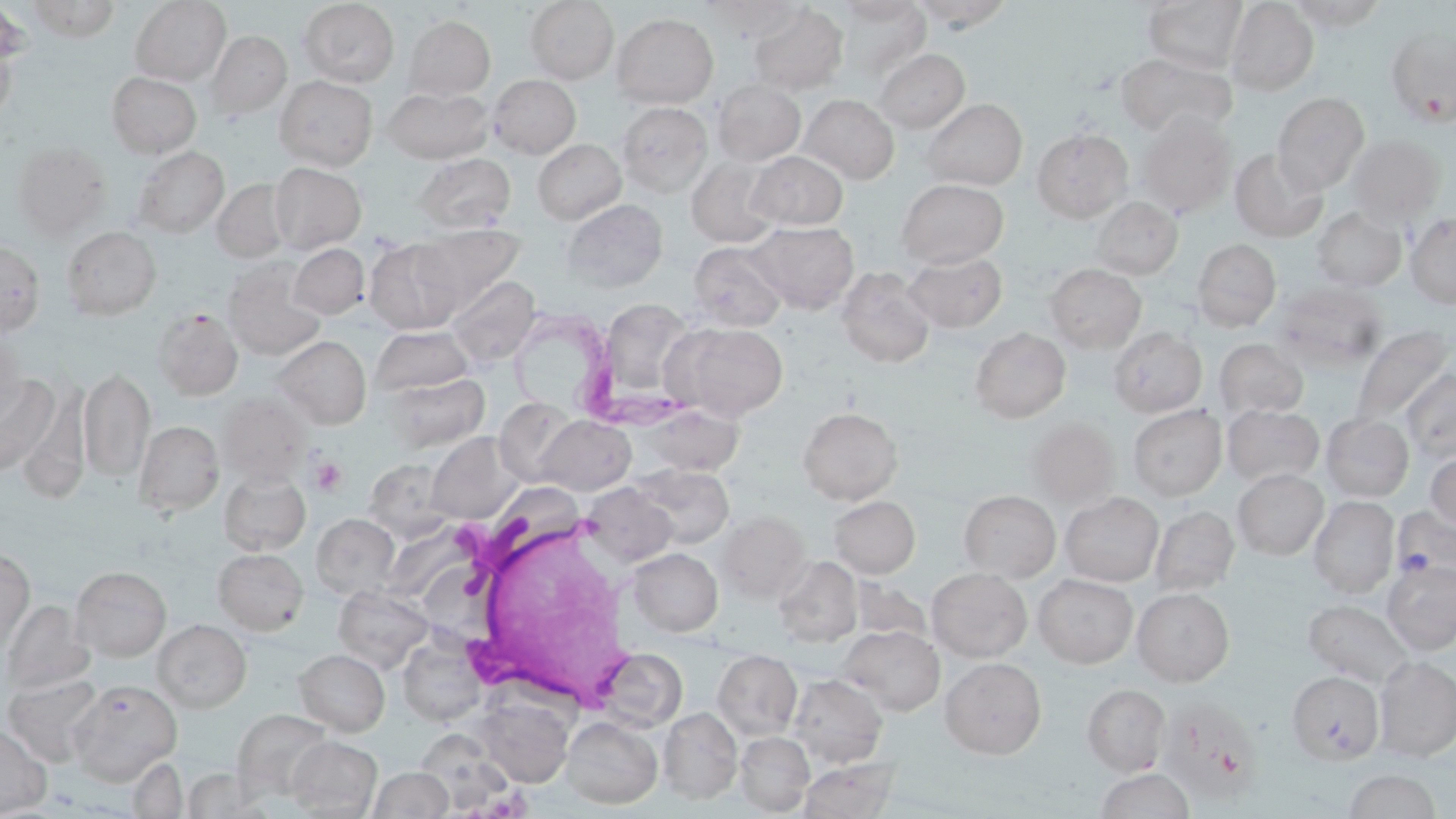
slide-level diagnosis = Trypanosoma brucei
preparation = thin blood film
image size = 1456×819 pixels
modality = optical microscopy
magnification = 1000x
uninfected red blood cell locations = approximate bounding boxes as (x1, y1, x2, y2) in pixels: (23, 0, 122, 41), (129, 0, 231, 85), (298, 0, 399, 87), (524, 0, 619, 84), (702, 0, 807, 42), (834, 0, 925, 23), (1142, 0, 1247, 74), (911, 1, 1014, 31), (1225, 1, 1319, 96), (1287, 1, 1388, 31), (1, 3, 31, 74), (834, 3, 931, 80), (748, 4, 848, 95), (611, 13, 719, 108), (404, 15, 496, 100), (0, 27, 18, 123), (1386, 28, 1456, 126), (206, 31, 292, 119), (874, 48, 970, 133), (1116, 52, 1237, 139), (106, 71, 202, 158), (488, 74, 581, 159), (274, 75, 378, 170), (712, 79, 806, 166), (383, 86, 494, 164), (1272, 92, 1370, 194), (800, 94, 899, 184), (922, 99, 1027, 189), (617, 101, 712, 197), (1137, 113, 1237, 217), (1032, 127, 1133, 222), (1347, 135, 1446, 224), (532, 138, 626, 224), (11, 142, 111, 239), (130, 145, 230, 239), (1230, 148, 1328, 243), (748, 151, 848, 230), (414, 152, 515, 233), (687, 157, 782, 246), (269, 162, 366, 253), (212, 178, 292, 263), (897, 179, 1009, 267), (1091, 196, 1183, 279), (562, 198, 668, 292), (1311, 206, 1406, 293), (1406, 213, 1456, 308), (747, 221, 859, 313), (412, 224, 525, 313), (62, 226, 161, 320), (364, 238, 463, 334), (1191, 238, 1281, 331), (0, 240, 45, 336), (688, 241, 788, 331), (289, 244, 369, 320), (903, 250, 1008, 331), (222, 259, 327, 360), (1045, 264, 1146, 352), (836, 266, 935, 369), (446, 275, 541, 367), (1273, 283, 1389, 375), (597, 298, 697, 405), (152, 308, 244, 400), (673, 323, 788, 420), (1351, 325, 1454, 427), (1109, 326, 1207, 417), (371, 327, 473, 396), (970, 327, 1071, 423), (0, 331, 26, 422), (272, 336, 371, 429), (1214, 338, 1308, 419), (77, 368, 155, 484), (1401, 368, 1456, 463), (384, 373, 489, 453), (0, 375, 59, 477), (16, 381, 92, 502), (218, 393, 310, 486), (494, 397, 580, 486), (639, 404, 744, 477), (1127, 404, 1227, 500), (1222, 404, 1324, 487), (798, 406, 903, 504), (1321, 413, 1414, 501), (536, 415, 636, 495), (1027, 419, 1120, 508), (134, 420, 224, 517), (427, 432, 521, 523), (1425, 448, 1456, 536), (363, 458, 455, 540), (633, 465, 734, 548), (1233, 468, 1328, 559), (219, 470, 311, 556), (582, 483, 677, 568), (959, 490, 1061, 582), (1061, 492, 1163, 586), (829, 495, 920, 578), (1309, 496, 1398, 597), (1149, 504, 1239, 596), (1390, 507, 1456, 585), (717, 511, 811, 603), (311, 513, 400, 599), (213, 548, 309, 635), (628, 548, 723, 636), (0, 549, 35, 654), (773, 555, 863, 647), (1383, 559, 1456, 654), (70, 566, 171, 661), (927, 568, 1032, 662), (1034, 574, 1137, 668), (851, 577, 932, 644), (333, 584, 434, 673), (1132, 588, 1234, 685), (1, 599, 94, 696), (1303, 599, 1415, 687), (152, 619, 251, 713), (839, 625, 945, 715), (398, 637, 486, 726), (596, 647, 687, 733), (294, 648, 390, 736), (712, 649, 802, 739), (1373, 656, 1456, 761), (940, 657, 1047, 758), (2, 671, 104, 766), (1288, 671, 1384, 764), (789, 674, 887, 768), (68, 679, 182, 784), (1082, 684, 1171, 776), (476, 697, 573, 788), (1164, 699, 1267, 806), (794, 702, 892, 815), (659, 707, 742, 803), (232, 709, 334, 800), (562, 716, 663, 809), (0, 722, 53, 817), (415, 730, 515, 815), (735, 731, 814, 815), (286, 735, 382, 817), (127, 757, 188, 818), (799, 759, 900, 819), (368, 766, 453, 819), (1095, 768, 1195, 819), (1342, 769, 1444, 818)
white blood cell locations = approximate bounding boxes as (x1, y1, x2, y2) in pixels: (432, 509, 641, 712)
stain = May-Grünwald-Giemsa
Trypanosoma brucei locations = approximate bounding boxes as (x1, y1, x2, y2) in pixels: (517, 308, 684, 430)
field of view = single
platelet locations = approximate bounding boxes as (x1, y1, x2, y2) in pixels: (310, 457, 348, 495)